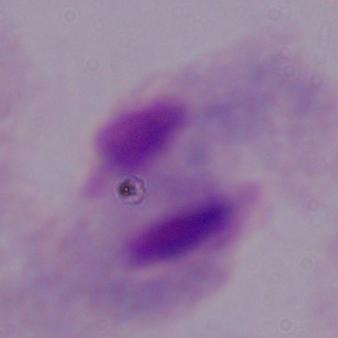 A trichomonad is seen. Micrograph. Captured at 1000x magnification.